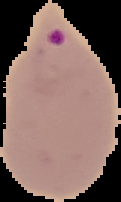
Summary:
  - Preparation: thin blood smear
  - Malaria status: parasitized
  - Image type: cell region segmented out of the field of view; surrounding area masked to black
  - Image size: 121×202 pixels